Classify this cell by malaria status.
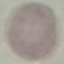
It is uninfected.

Summary:
  - Capture: smartphone through the microscope eyepiece
  - Preparation: thin smear
  - Stain: Giemsa
  - Image type: cell patch, automatically extracted from a larger field of view and resized to 64 × 64 pixels